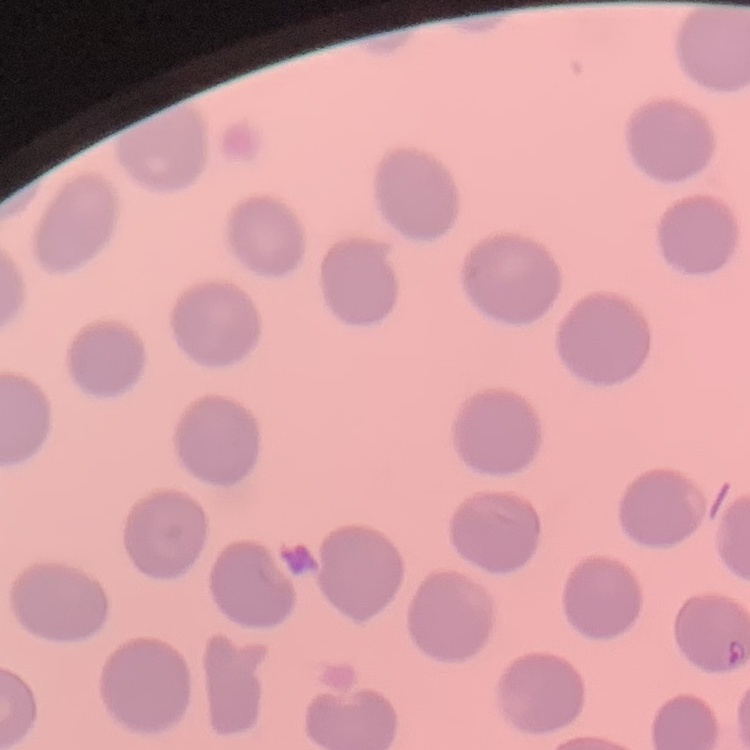
erythrocyte morphology = no rouleaux formation
stain = Field's or Giemsa
preparation = thin blood smear
image type = square crop of a larger photomicrograph